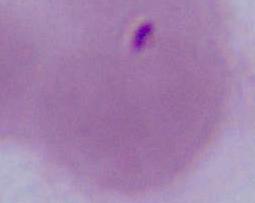

identification: erythrocyte
magnification: 1000x
modality: micrograph